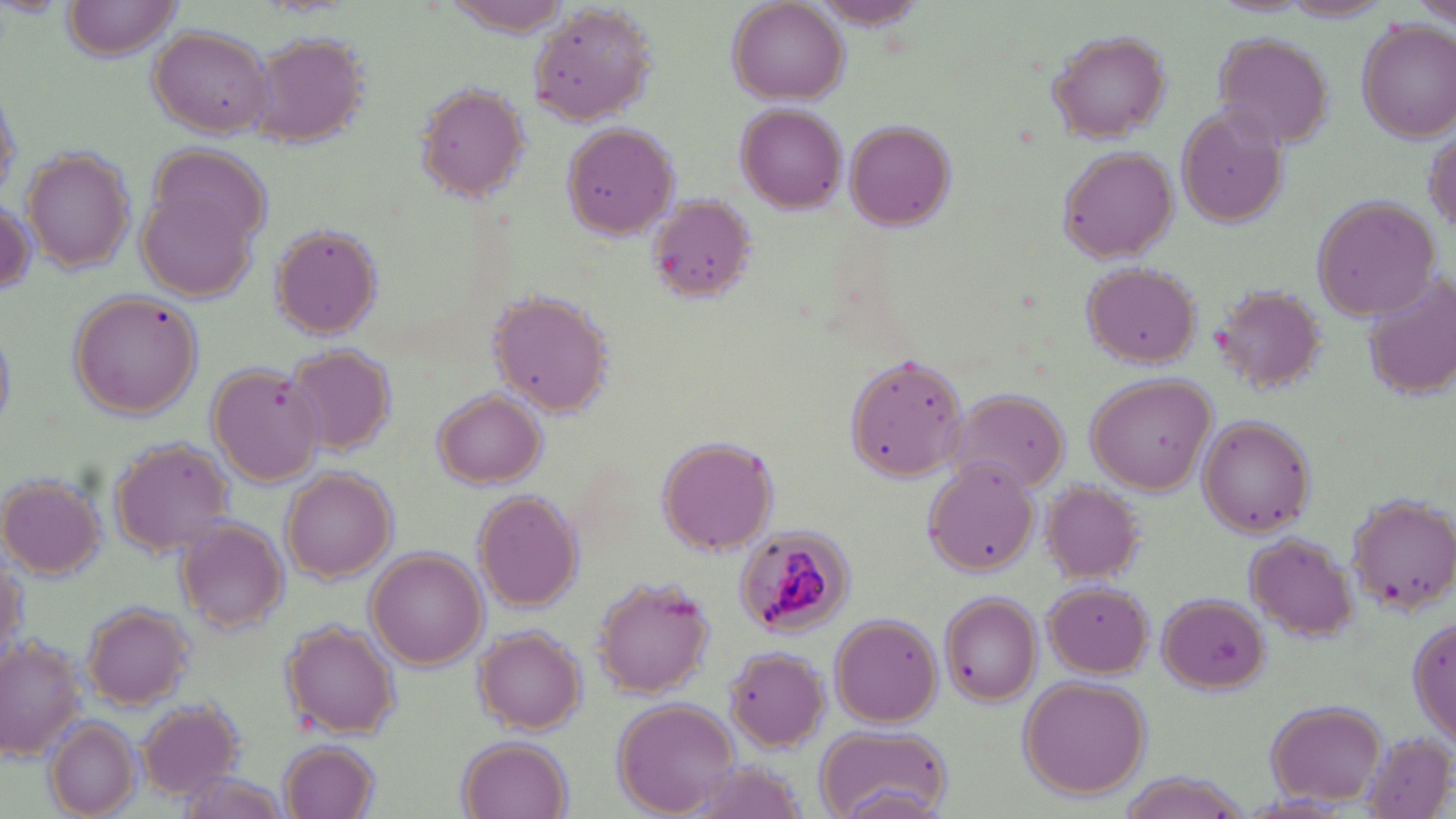
Approximate bounding boxes as named x1/y1/x2/y2 corners in pixels. Uninfected red blood cell locations: (x1=62, y1=0, x2=185, y2=59), (x1=1414, y1=0, x2=1456, y2=31), (x1=438, y1=1, x2=573, y2=36), (x1=727, y1=1, x2=849, y2=106), (x1=810, y1=1, x2=930, y2=29), (x1=1279, y1=1, x2=1394, y2=22), (x1=526, y1=5, x2=658, y2=127), (x1=1359, y1=20, x2=1456, y2=141), (x1=148, y1=25, x2=275, y2=138), (x1=1045, y1=29, x2=1172, y2=143), (x1=251, y1=33, x2=370, y2=149), (x1=1213, y1=33, x2=1335, y2=150), (x1=415, y1=81, x2=531, y2=205), (x1=0, y1=82, x2=25, y2=204), (x1=736, y1=103, x2=846, y2=213), (x1=1176, y1=106, x2=1288, y2=229), (x1=843, y1=118, x2=958, y2=232), (x1=562, y1=122, x2=681, y2=241), (x1=1424, y1=123, x2=1455, y2=240), (x1=1056, y1=147, x2=1177, y2=262), (x1=23, y1=149, x2=135, y2=274), (x1=142, y1=160, x2=270, y2=303), (x1=648, y1=194, x2=756, y2=302), (x1=1310, y1=194, x2=1440, y2=320), (x1=2, y1=198, x2=37, y2=297), (x1=270, y1=223, x2=385, y2=339), (x1=1080, y1=261, x2=1202, y2=369), (x1=1364, y1=272, x2=1456, y2=399), (x1=1209, y1=283, x2=1330, y2=395), (x1=69, y1=291, x2=205, y2=418), (x1=489, y1=291, x2=613, y2=417), (x1=0, y1=324, x2=15, y2=436), (x1=284, y1=343, x2=397, y2=454), (x1=843, y1=354, x2=971, y2=481), (x1=211, y1=366, x2=326, y2=485), (x1=1086, y1=373, x2=1215, y2=495), (x1=948, y1=390, x2=1069, y2=492), (x1=434, y1=391, x2=545, y2=487), (x1=1198, y1=417, x2=1316, y2=535), (x1=655, y1=435, x2=780, y2=556), (x1=110, y1=439, x2=231, y2=555), (x1=923, y1=458, x2=1040, y2=575), (x1=282, y1=468, x2=396, y2=582), (x1=0, y1=473, x2=107, y2=580), (x1=1040, y1=480, x2=1147, y2=584), (x1=473, y1=490, x2=585, y2=611), (x1=1349, y1=494, x2=1456, y2=615), (x1=178, y1=517, x2=288, y2=633), (x1=1245, y1=533, x2=1359, y2=639), (x1=368, y1=549, x2=487, y2=669), (x1=0, y1=553, x2=25, y2=663), (x1=592, y1=576, x2=715, y2=697), (x1=1045, y1=579, x2=1155, y2=678), (x1=1157, y1=591, x2=1268, y2=694), (x1=939, y1=592, x2=1040, y2=707), (x1=83, y1=603, x2=192, y2=708), (x1=1409, y1=612, x2=1454, y2=750), (x1=830, y1=613, x2=943, y2=726), (x1=283, y1=621, x2=401, y2=740), (x1=473, y1=624, x2=585, y2=733), (x1=0, y1=635, x2=82, y2=760), (x1=724, y1=645, x2=832, y2=751), (x1=1018, y1=675, x2=1152, y2=799), (x1=1264, y1=697, x2=1387, y2=804), (x1=613, y1=699, x2=740, y2=815), (x1=137, y1=700, x2=243, y2=800), (x1=48, y1=718, x2=140, y2=818), (x1=816, y1=724, x2=951, y2=819), (x1=1362, y1=731, x2=1453, y2=817), (x1=456, y1=737, x2=573, y2=819), (x1=278, y1=739, x2=382, y2=819), (x1=680, y1=759, x2=812, y2=818), (x1=171, y1=769, x2=292, y2=819), (x1=1113, y1=772, x2=1252, y2=819). Plasmodium malariae-infected red blood cell locations: (x1=734, y1=526, x2=855, y2=639). Slide-level diagnosis: Plasmodium malariae. Optical microscopy. Image is 1456×819 pixels. Thin blood film. Captured at 1000x magnification. Single field of view. May-Grünwald-Giemsa stain.